Identify the preparation type.
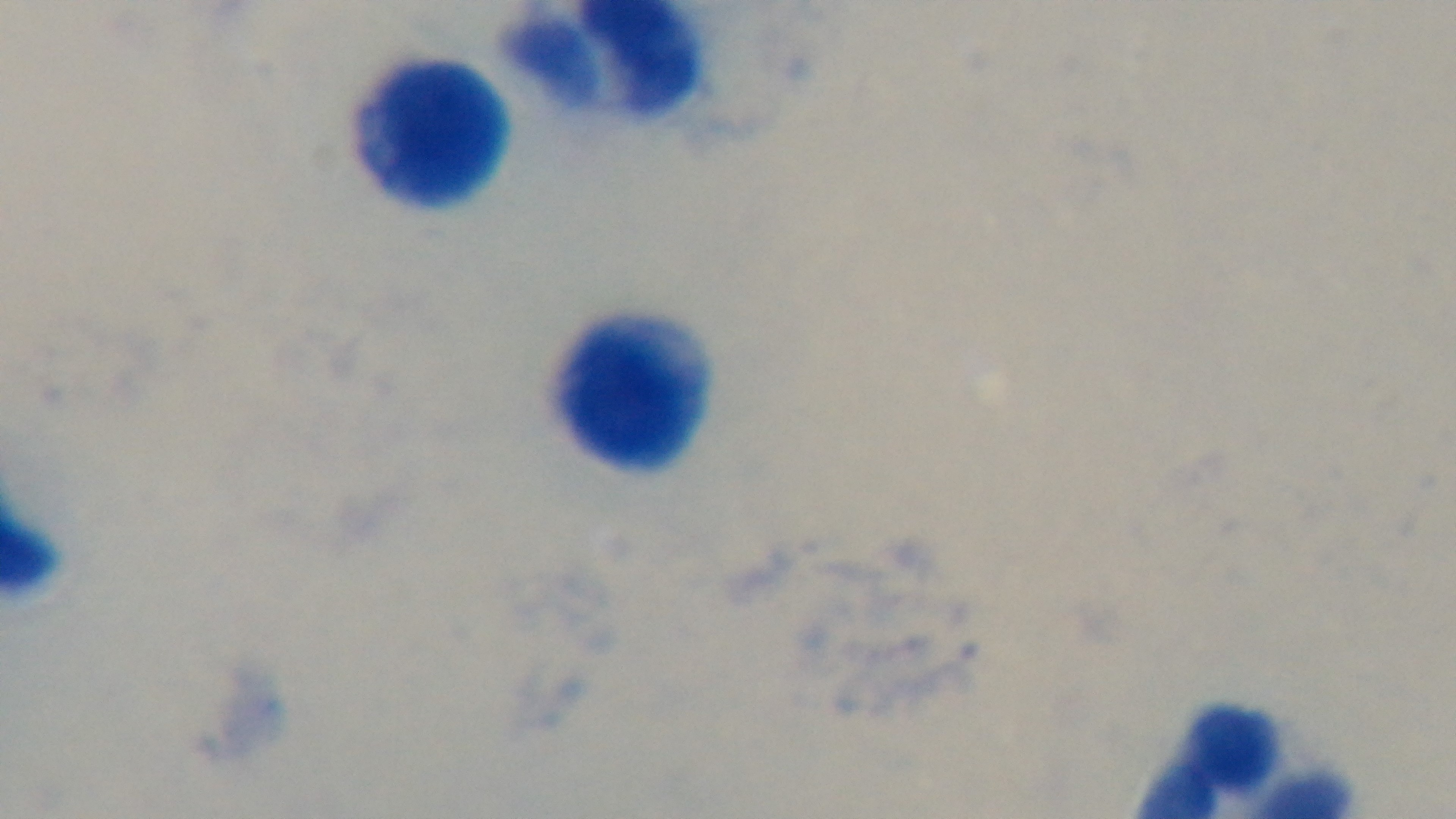
Thick.

{
  "objective": "100x oil immersion",
  "stain": "Giemsa",
  "field_of_view": "single",
  "modality": "light microscopy",
  "malaria_status": "negative",
  "capture": "mounted 4K digital camera"
}